Name the cell type shown.
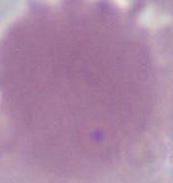

An erythrocyte.

magnification = 1000x
modality = photomicrograph